Locate every Plasmodium falciparum-infected red blood cell.
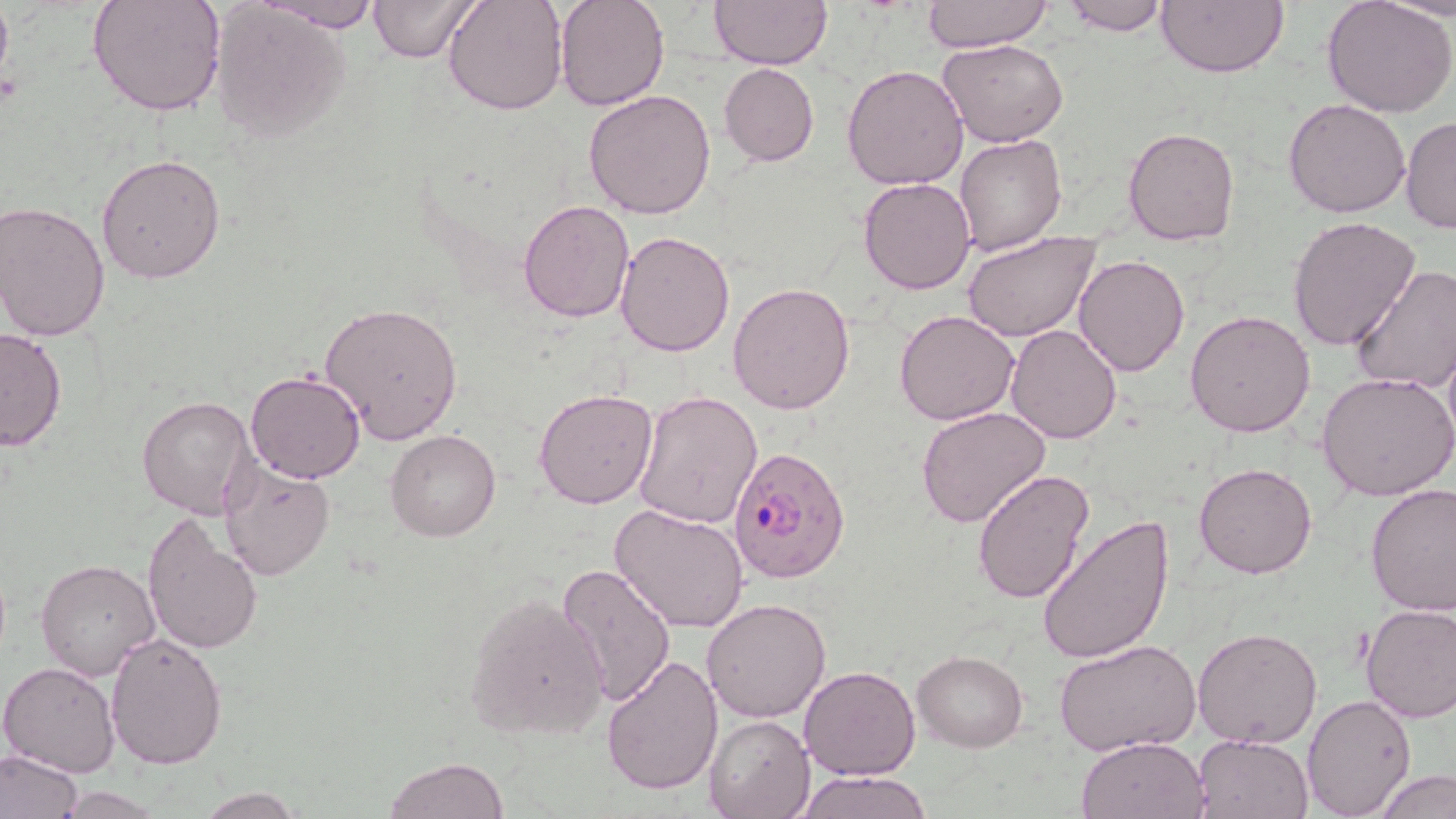

Approximate bounding boxes as [x1, y1, x2, y2] in pixels.
Plasmodium falciparum-infected red blood cells: [729, 445, 852, 582].

Uninfected red blood cell locations: [87, 0, 226, 118], [258, 0, 386, 31], [368, 0, 476, 62], [444, 0, 567, 115], [554, 0, 669, 110], [711, 0, 833, 71], [924, 0, 1054, 52], [1060, 0, 1172, 36], [1156, 0, 1289, 77], [1323, 0, 1456, 118], [1381, 0, 1456, 22], [211, 3, 352, 141], [939, 38, 1068, 146], [719, 63, 819, 165], [841, 64, 967, 190], [582, 89, 716, 219], [1283, 98, 1413, 219], [1401, 114, 1456, 234], [1122, 128, 1239, 245], [954, 135, 1068, 256], [96, 153, 226, 285], [858, 176, 977, 294], [518, 198, 634, 321], [1, 200, 113, 342], [1289, 217, 1421, 355], [615, 229, 737, 356], [961, 232, 1100, 344], [1074, 253, 1190, 376], [1349, 264, 1456, 394], [727, 282, 856, 415], [318, 302, 464, 444], [895, 310, 1020, 425], [1185, 310, 1316, 437], [1006, 324, 1123, 443], [0, 327, 68, 452], [245, 370, 365, 484], [1318, 371, 1456, 503], [534, 389, 658, 510], [634, 390, 763, 526], [137, 395, 255, 520], [916, 405, 1051, 529], [387, 430, 500, 542], [218, 457, 336, 581], [1194, 463, 1317, 578], [974, 467, 1094, 605], [1365, 483, 1456, 616], [610, 503, 749, 632], [142, 511, 263, 657], [1035, 514, 1174, 664], [36, 560, 161, 681], [553, 562, 675, 709], [464, 593, 611, 742], [702, 597, 832, 722], [1360, 603, 1456, 724], [1193, 626, 1323, 748], [105, 632, 228, 770], [1055, 638, 1199, 756], [913, 650, 1027, 751], [602, 653, 725, 797], [1, 662, 121, 779], [798, 665, 920, 780], [1301, 694, 1415, 817], [704, 714, 815, 819], [1193, 733, 1312, 818], [1076, 735, 1207, 819], [0, 749, 86, 819], [384, 757, 510, 818], [1376, 769, 1456, 819], [796, 771, 934, 819], [193, 788, 306, 818]. Slide-level diagnosis: Plasmodium falciparum. Thin blood smear. Captured at 1000x magnification. May-Grünwald-Giemsa-stained preparation. Single field of view. Image is 1456×819 pixels. Light microscopy.